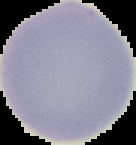
Summary:
  - Image type: segmented cell region with the area outside set to black
  - Image size: 136×145 pixels
  - Result: no Plasmodium parasites detected
  - Preparation: thin blood smear